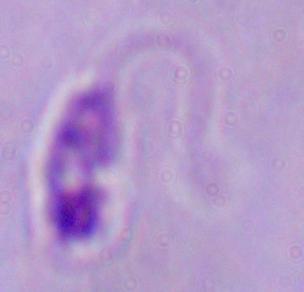 A Leishmania parasite is seen. Photomicrograph. 1000x magnification.